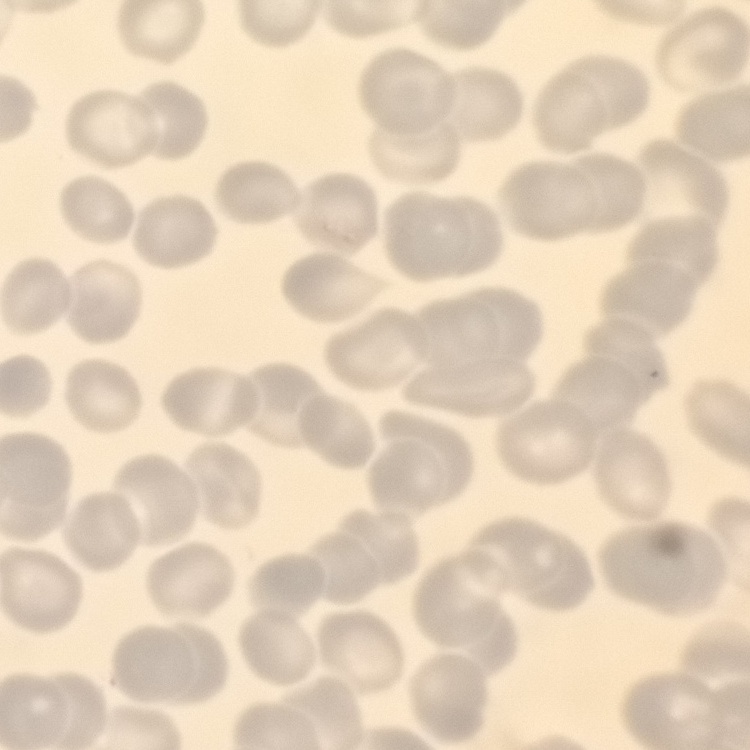

The red blood cells exhibit no rouleaux formation. Stained with either Field's or Giemsa. One tile cut from a larger photomicrograph. Thin blood film.